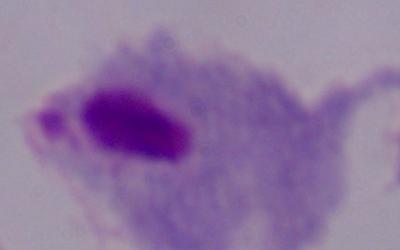

Summary:
  - Identification: trichomonad
  - Magnification: 1000x
  - Modality: micrograph